Name the parasite shown.
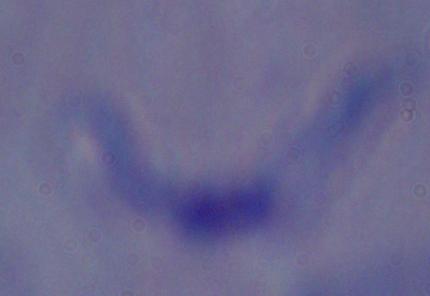
A trypanosome.

Summary:
  - Magnification: 1000x
  - Modality: micrograph